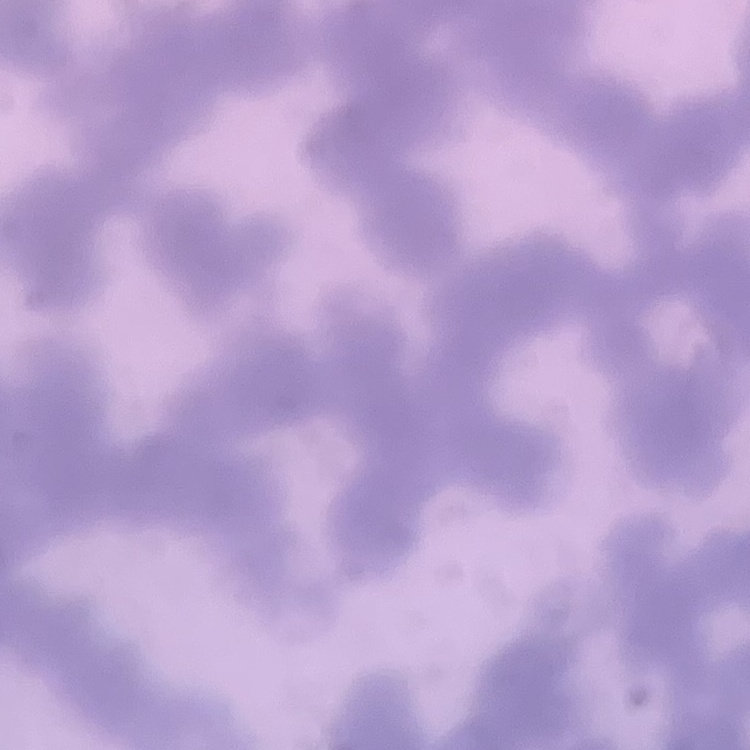

red blood cell morphology = rouleaux formation
stain = Field's or Giemsa
preparation = thin blood smear
image type = one tile cut from a larger photomicrograph